Report the malaria status of this cell.
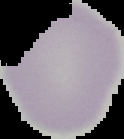

Uninfected.

Summary:
  - Image type: segmented cell region on a black background
  - Preparation: thin blood film
  - Image size: 124×139 pixels